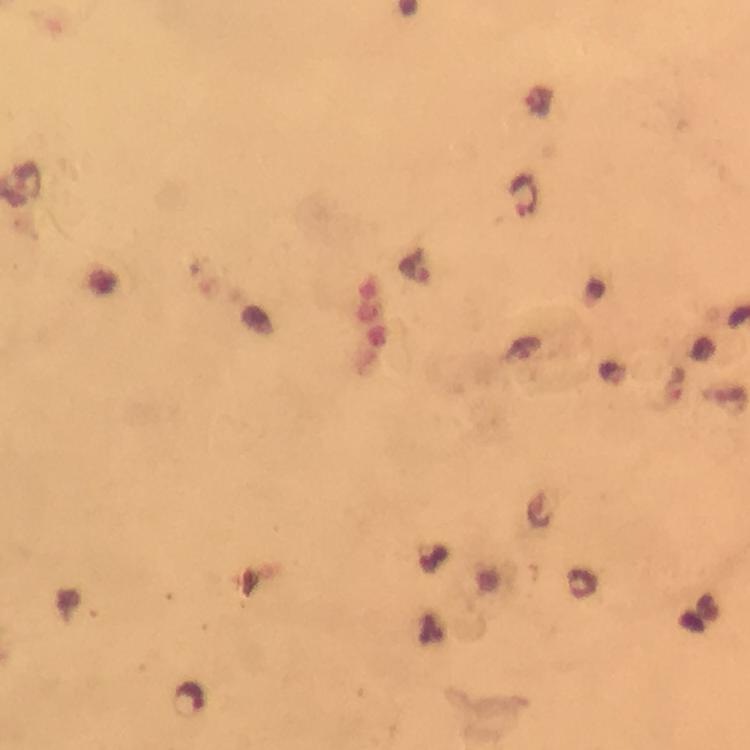

Approximate centers as (x, y) in pixels. Malaria parasite locations: (525, 194), (189, 700). Immersion oil was used. From a malaria diagnostic workup. Thick smear. Smartphone photograph taken through a microscope. Giemsa-stained preparation. A crop from one field of view. Image is 750×750 pixels. 100x magnification.